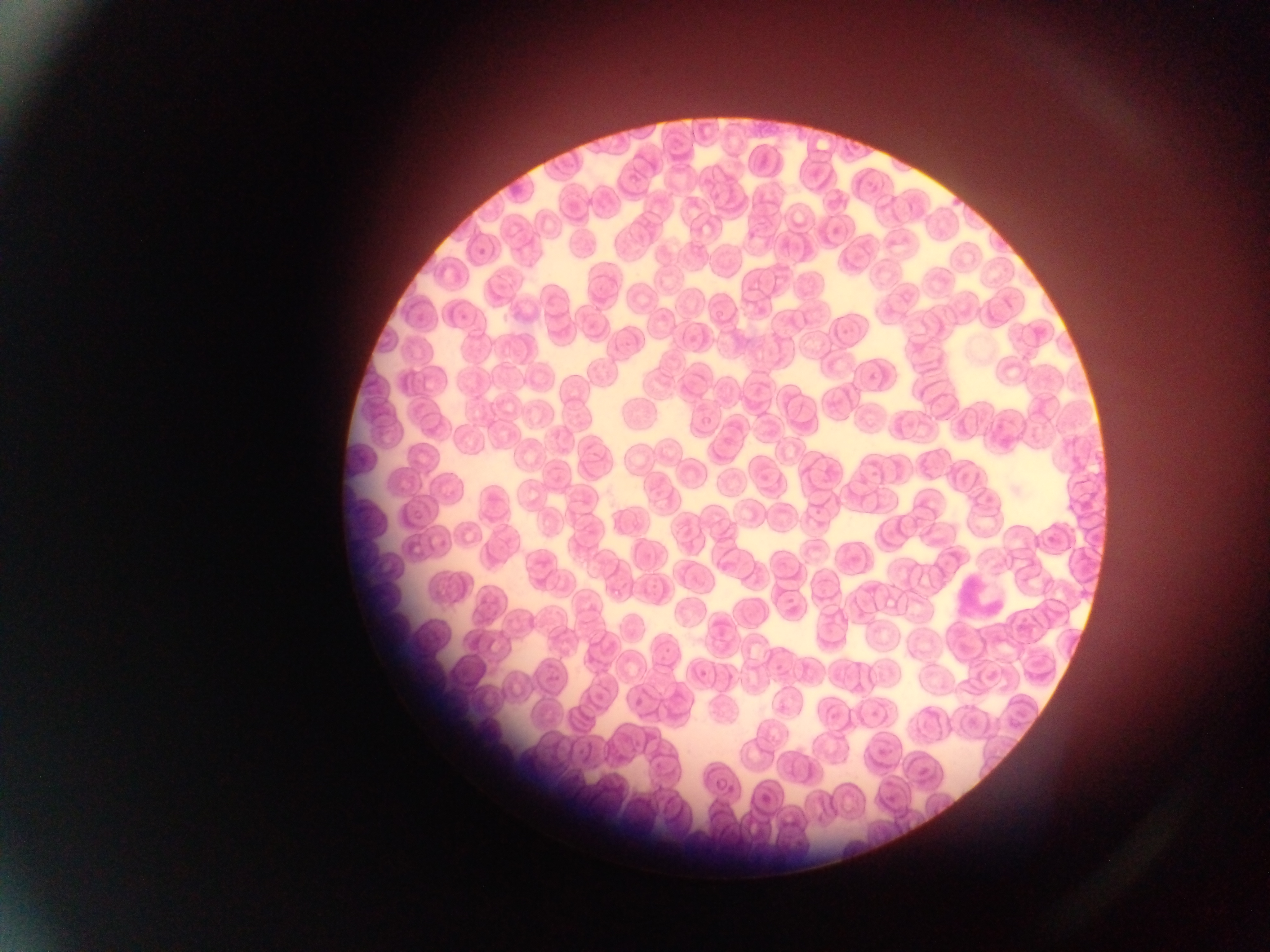

Approximate bounding boxes as [left, top, right, bottom] in pixels. Leukocyte locations: [951, 567, 1015, 620]. Single field of view. Image is 1270×952 pixels. Thin blood smear. Sample from Ghana. Mobile-phone photograph taken through the microscope.